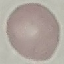
result = no malaria parasites seen
preparation = thin smear
capture = smartphone camera at the microscope eyepiece
image type = cell patch, automatically extracted from a larger field of view and resized to 64 × 64 pixels
stain = Giemsa